Locate every Plasmodium parasite.
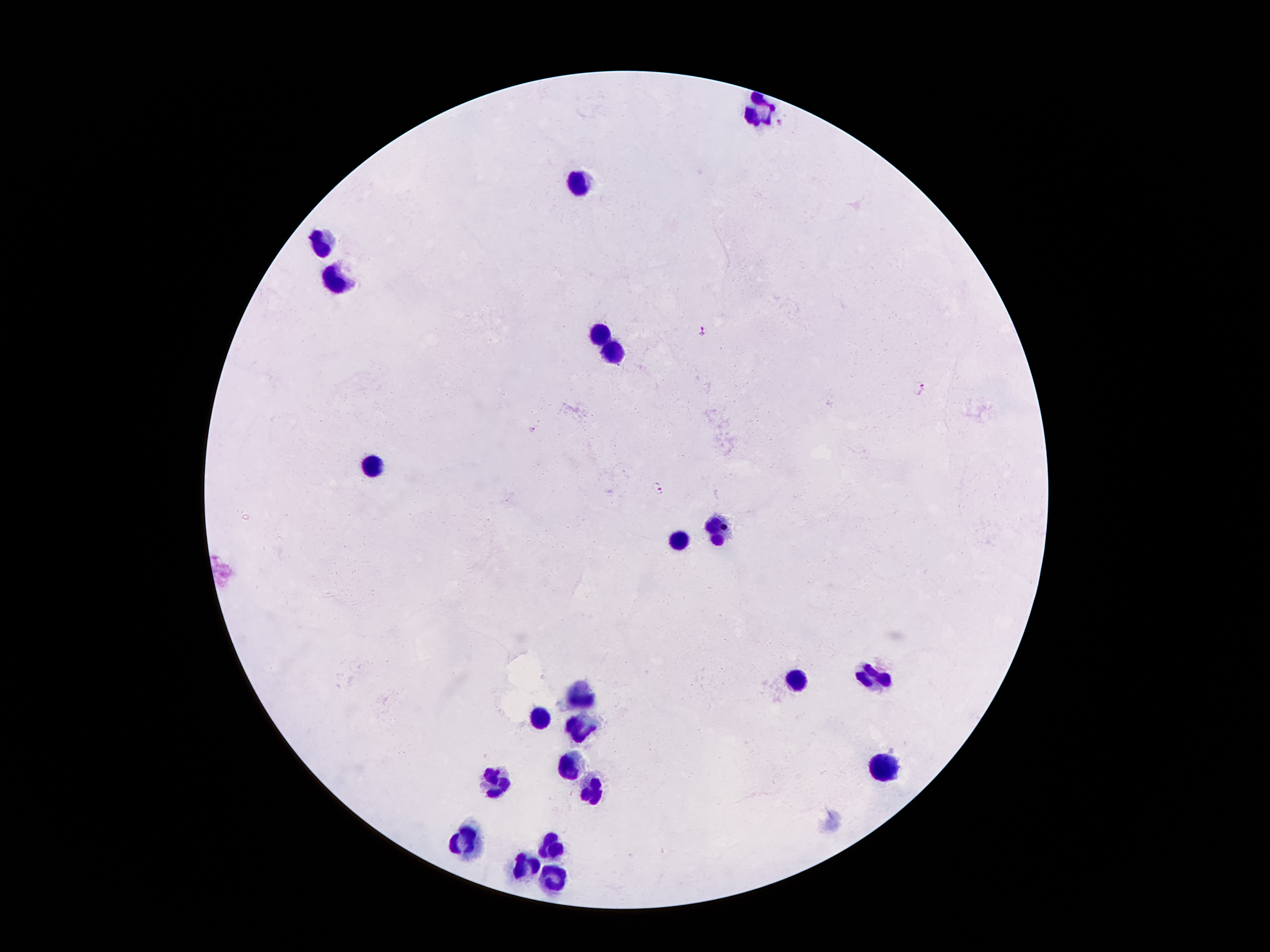
Approximate centers as [x, y] in pixels.
Plasmodium parasites: [778, 122], [701, 331], [919, 387], [533, 428], [659, 489].

Leukocyte locations: [751, 113], [578, 186], [320, 241], [339, 281], [601, 331], [612, 352], [375, 461], [715, 533], [677, 541], [799, 682], [870, 682], [580, 694], [541, 717], [580, 722], [574, 764], [883, 768], [496, 782], [593, 791], [469, 837], [553, 843], [526, 864], [553, 879]. Giemsa-stained preparation. Single field of view. 100x magnification. Patient malaria status: infected with Plasmodium falciparum. Thick blood smear. Smartphone photograph taken through the microscope eyepiece. Image is 1270×952 pixels.